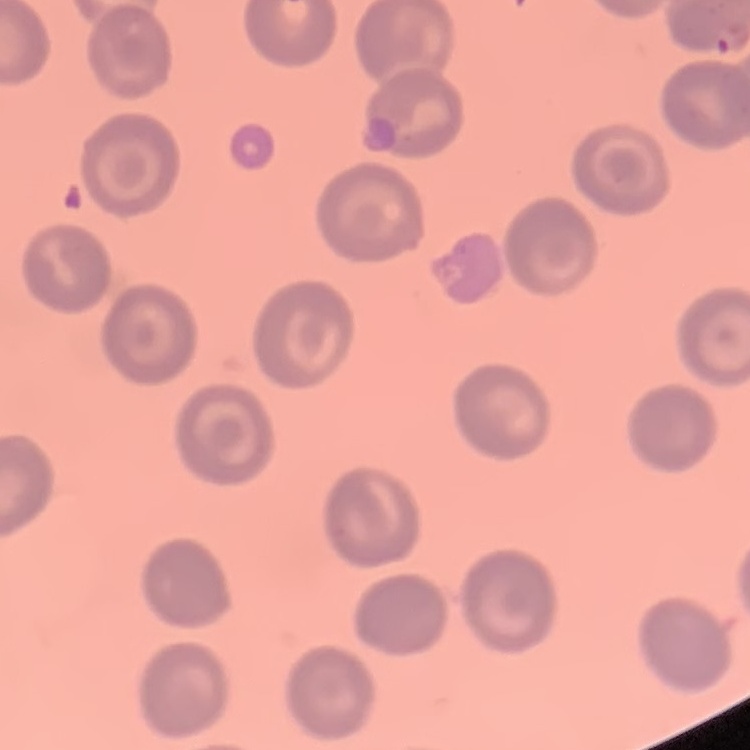
{
  "red_blood_cell_morphology": "no rouleaux formation",
  "preparation": "thin blood smear",
  "stain": "Field's or Giemsa",
  "image_type": "one tile cut from a larger photomicrograph"
}